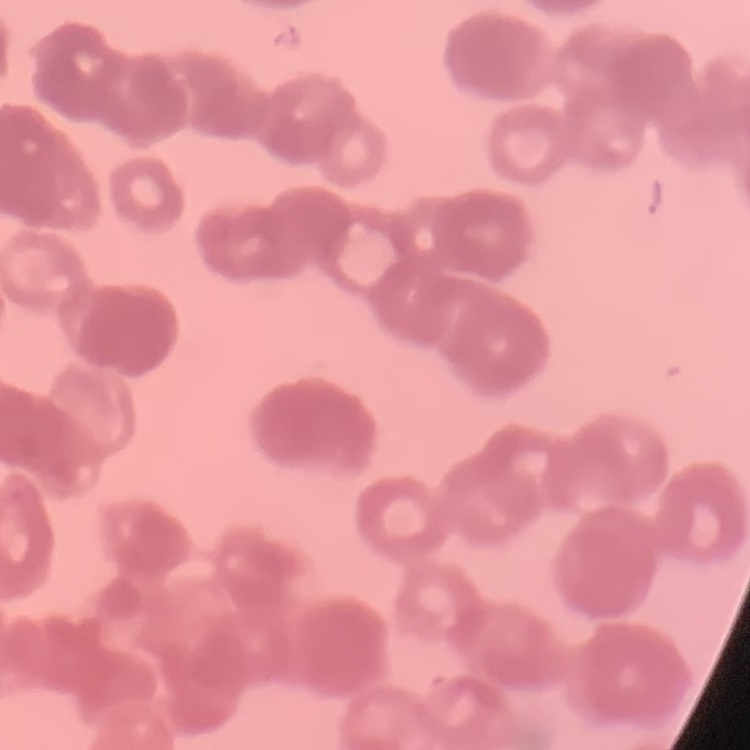

Summary:
  - Erythrocyte morphology: rouleaux formation
  - Image type: square crop of a larger photomicrograph
  - Preparation: thin blood smear
  - Stain: Field's or Giemsa